Describe the morphology of the red blood cells.
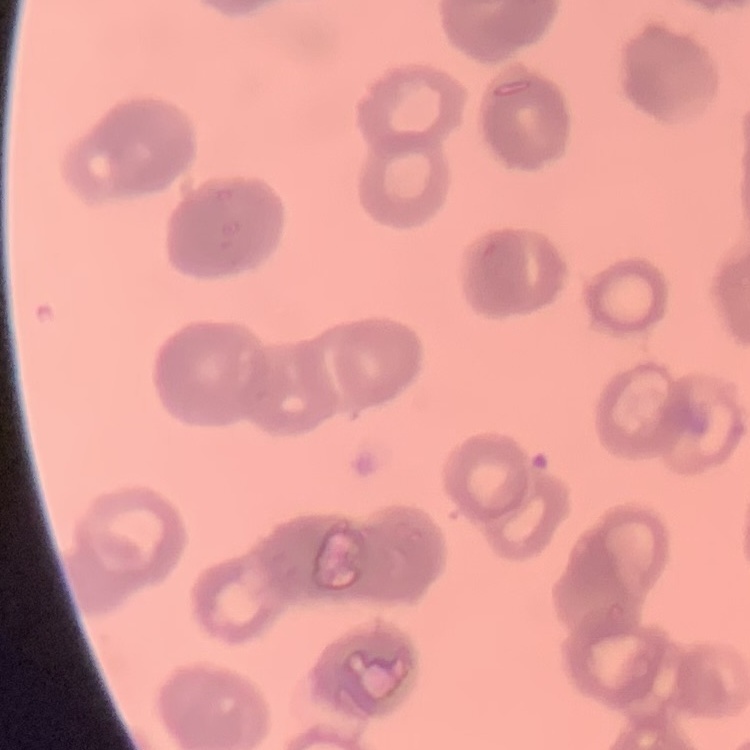

Rouleaux formation.

Thin blood smear. One tile cut from a larger photomicrograph. Field's or Giemsa stain.